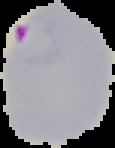
{
  "result": "Plasmodium parasites detected",
  "preparation": "thin blood film",
  "image_type": "segmented cell region with the area outside set to black",
  "image_size": "115×148 pixels"
}